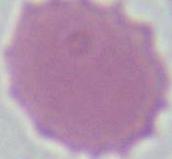

Captured at 1000x magnification. Micrograph. A red blood cell is shown.